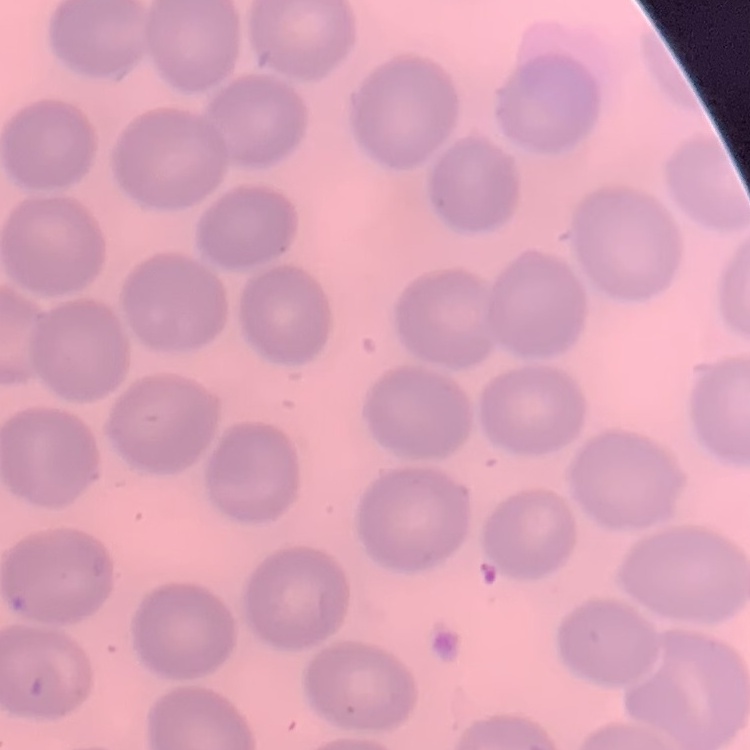

The erythrocytes exhibit no rouleaux formation. Field's or Giemsa stain. One tile cut from a larger photomicrograph. Thin peripheral smear.